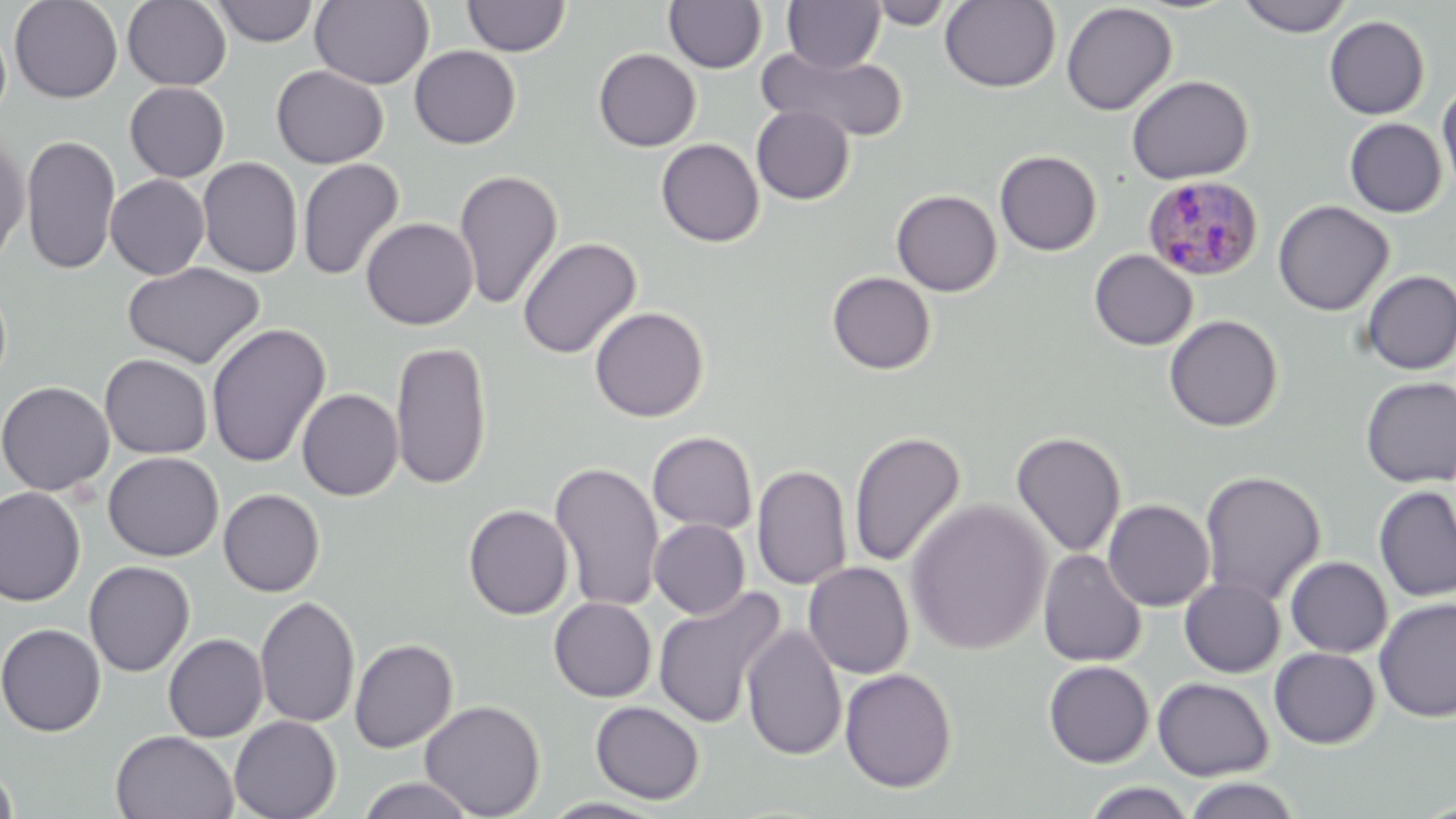

slide_level_diagnosis: Plasmodium malariae
field_of_view: single
preparation: thin blood smear
image_size: 1456×819 pixels
uninfected_red_blood_cell_locations: 'approximate bounding boxes as [x1, y1, x2, y2] in pixels: [9, 0, 123, 103], [122, 0, 232, 90], [310, 0, 434, 89], [462, 0, 571, 57], [664, 0, 767, 73], [867, 0, 956, 29], [940, 0, 1061, 93], [1236, 0, 1353, 37], [211, 1, 318, 46], [782, 1, 886, 73], [1061, 3, 1178, 116], [1324, 15, 1430, 120], [0, 17, 12, 127], [409, 45, 521, 149], [756, 46, 910, 143], [593, 48, 701, 151], [271, 65, 389, 168], [1126, 74, 1253, 184], [1437, 80, 1456, 202], [124, 81, 230, 182], [751, 105, 855, 205], [1344, 118, 1448, 218], [21, 134, 121, 275], [0, 135, 30, 268], [656, 138, 764, 247], [995, 150, 1102, 256], [197, 157, 304, 278], [297, 158, 405, 281], [453, 169, 563, 310], [105, 174, 210, 280], [891, 189, 1002, 296], [1273, 200, 1394, 316], [360, 217, 478, 330], [516, 237, 641, 360], [1089, 249, 1198, 350], [123, 261, 266, 369], [1359, 270, 1456, 375], [826, 271, 936, 375], [589, 306, 709, 422], [1164, 314, 1283, 432], [206, 322, 331, 469], [390, 340, 493, 490], [100, 354, 213, 458], [1359, 376, 1456, 487], [1, 380, 114, 496], [297, 388, 404, 501], [848, 430, 965, 568], [647, 431, 758, 534], [1011, 431, 1126, 559], [103, 452, 223, 561], [549, 461, 665, 613], [751, 464, 853, 590], [1048, 470, 1153, 589], [1199, 470, 1326, 605], [1374, 485, 1456, 601], [0, 486, 85, 606], [218, 488, 325, 596], [905, 499, 1052, 655], [1103, 499, 1215, 611], [463, 504, 574, 620], [649, 518, 750, 619], [1037, 549, 1147, 667], [1285, 556, 1393, 658], [84, 561, 195, 677], [803, 562, 914, 679], [1179, 578, 1285, 677], [652, 586, 786, 730], [255, 595, 360, 729], [549, 597, 657, 702], [1373, 597, 1456, 723], [742, 622, 847, 761], [0, 623, 106, 736], [163, 634, 268, 742], [349, 638, 458, 753], [1269, 647, 1380, 749], [1043, 660, 1154, 768], [839, 667, 958, 793], [1153, 677, 1274, 781], [420, 699, 545, 818], [591, 700, 705, 804], [229, 715, 341, 819], [111, 730, 239, 818], [0, 762, 18, 819], [356, 776, 478, 819], [1181, 776, 1302, 818], [1081, 781, 1198, 819], [540, 797, 668, 818]'
plasmodium_malariae_infected_red_blood_cell_locations: 'approximate bounding boxes as [x1, y1, x2, y2] in pixels: [1144, 175, 1264, 281]'
magnification: 1000x
modality: light microscopy
stain: May-Grünwald-Giemsa